Identify the cell.
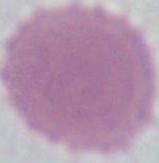
This is an erythrocyte.

Summary:
  - Magnification: 1000x
  - Modality: photomicrograph